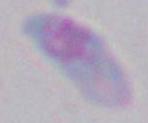

modality = photomicrograph
identification = Toxoplasma gondii
magnification = 1000x